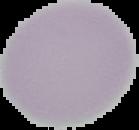
{
  "preparation": "thin blood film",
  "image_size": "139×130 pixels",
  "image_type": "segmented cell region on a black background",
  "malaria_status": "uninfected"
}